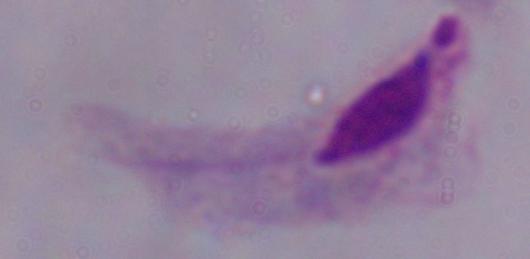
magnification = 1000x
identification = trichomonad
modality = photomicrograph